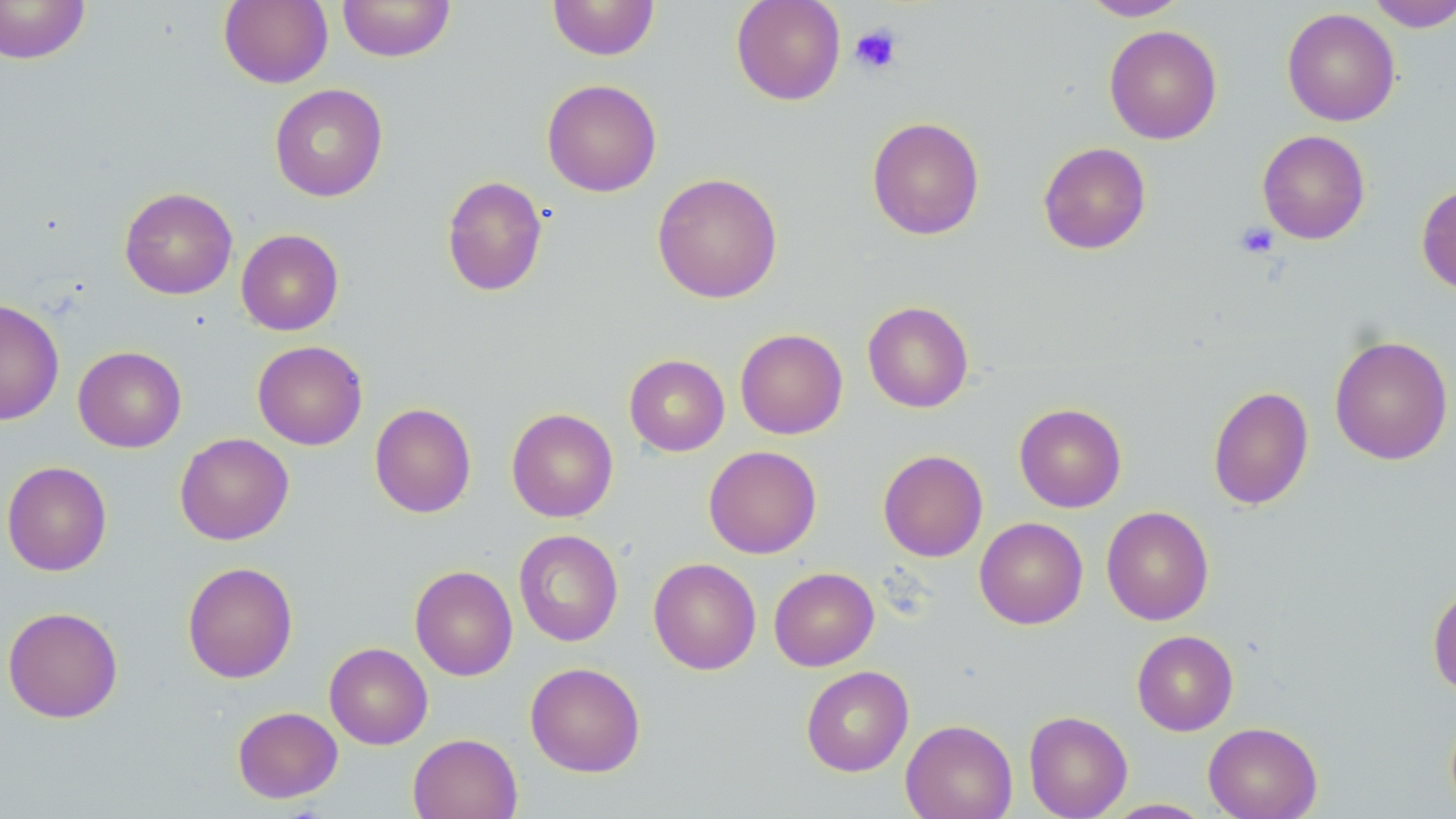

slide-level diagnosis = negative for blood parasites
platelet locations = approximate bounding boxes as [x1, y1, x2, y2] in pixels: [849, 23, 903, 74], [1235, 222, 1279, 259]
stain = May-Grünwald-Giemsa
magnification = 1000x
image size = 1456×819 pixels
modality = light microscopy
uninfected red blood cell locations = approximate bounding boxes as [x1, y1, x2, y2] in pixels: [219, 0, 333, 88], [337, 0, 455, 62], [547, 0, 660, 60], [731, 0, 846, 105], [1079, 0, 1189, 21], [1364, 0, 1456, 31], [0, 1, 92, 65], [1282, 7, 1401, 126], [1104, 25, 1222, 144], [542, 79, 662, 197], [269, 83, 388, 202], [866, 116, 984, 240], [1257, 130, 1370, 244], [1038, 142, 1151, 254], [652, 172, 783, 303], [441, 174, 548, 297], [1416, 183, 1456, 296], [119, 187, 237, 299], [236, 229, 344, 335], [0, 298, 65, 425], [862, 301, 974, 413], [735, 328, 848, 439], [1329, 335, 1454, 465], [252, 340, 367, 450], [73, 346, 186, 452], [624, 354, 730, 456], [1207, 386, 1314, 510], [369, 403, 476, 518], [1014, 403, 1127, 512], [506, 408, 618, 522], [175, 432, 293, 545], [703, 445, 822, 559], [878, 449, 988, 562], [2, 461, 112, 576], [1101, 505, 1214, 625], [974, 517, 1088, 629], [513, 529, 623, 646], [648, 558, 761, 674], [182, 561, 298, 683], [410, 565, 518, 681], [769, 567, 879, 671], [1427, 582, 1456, 696], [2, 606, 123, 723], [1132, 630, 1239, 736], [324, 642, 433, 749], [525, 661, 646, 777], [801, 665, 914, 777], [232, 706, 343, 803], [1023, 710, 1133, 819], [901, 719, 1017, 819], [1204, 722, 1322, 819], [407, 733, 523, 819], [1102, 798, 1215, 818]
field of view = single
preparation = thin blood smear